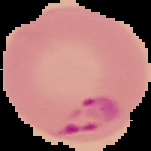
result = malaria parasites identified
image size = 151×151 pixels
preparation = thin blood film
image type = segmented cell region with the area outside set to black